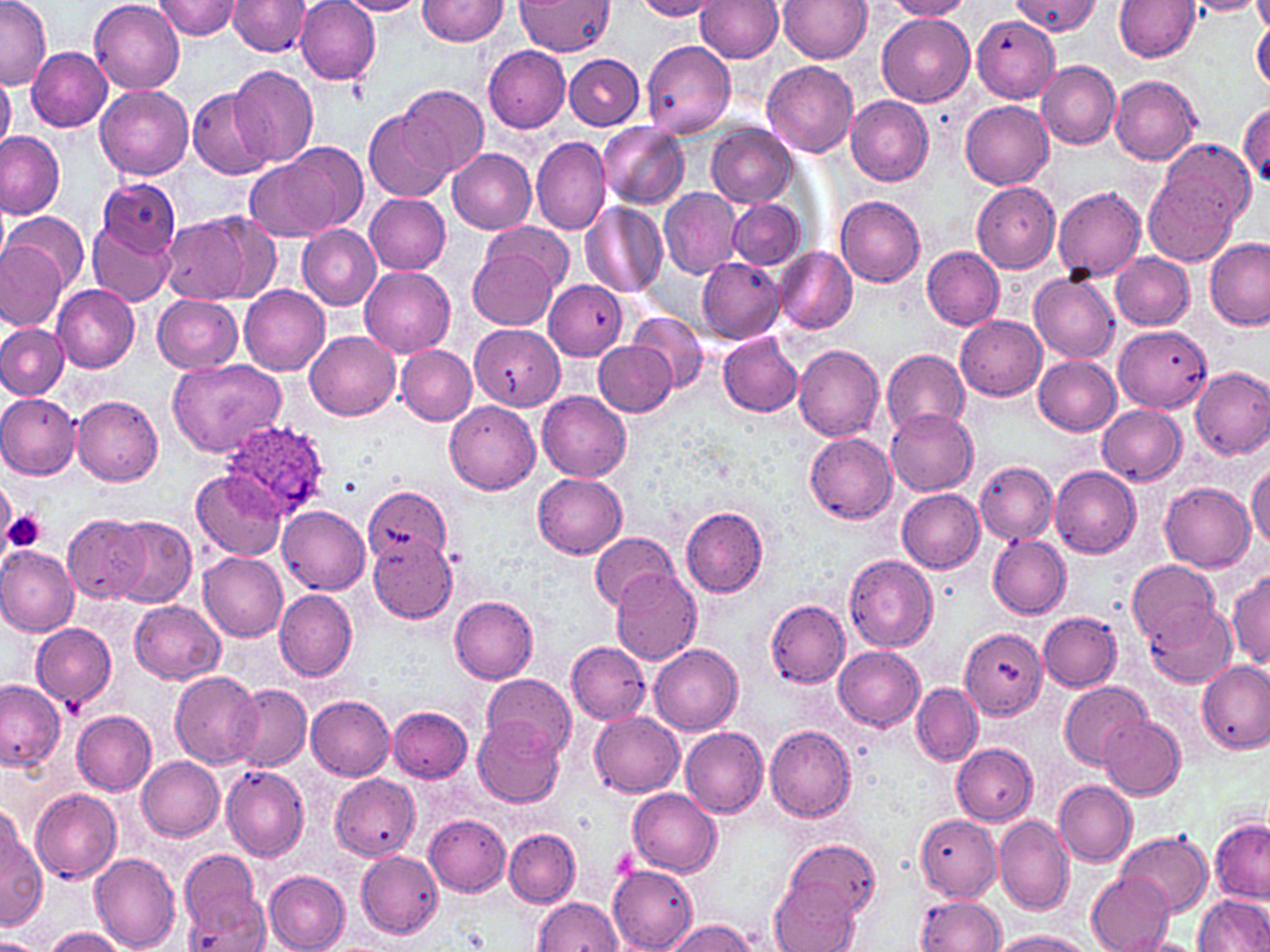
Summary:
  - Coordinate format: approximate bounding boxes as (x1,y1)-(x2,y2) corner pairs in pixels
  - Platelet locations: (0,480)-(15,544), (4,509)-(47,552), (609,845)-(638,883)
  - Plasmodium ovale-infected red blood cell locations: (221,418)-(332,520)
  - Uninfected red blood cell locations: (0,0)-(50,88), (90,0)-(184,93), (157,0)-(239,40), (296,0)-(380,84), (419,0)-(509,46), (517,0)-(614,56), (635,0)-(724,21), (778,0)-(873,63), (883,0)-(977,20), (1014,0)-(1100,35), (1114,0)-(1200,62), (1187,0)-(1267,17), (1253,0)-(1270,34), (229,1)-(310,57), (338,1)-(424,17), (697,1)-(784,62), (877,11)-(975,106), (972,15)-(1059,102), (1251,19)-(1270,90), (641,40)-(737,138), (26,46)-(114,131), (484,46)-(570,132), (565,53)-(643,129), (762,60)-(858,158), (1035,60)-(1120,149), (228,66)-(318,167), (0,73)-(16,148), (1110,74)-(1202,166), (97,84)-(194,180), (396,84)-(487,178), (189,89)-(275,178), (846,95)-(934,185), (961,101)-(1054,190), (1237,101)-(1269,181), (365,110)-(455,201), (596,121)-(689,208), (707,124)-(796,207), (0,132)-(65,218), (530,136)-(611,236), (280,142)-(367,232), (448,148)-(536,234), (245,155)-(346,243), (1145,157)-(1249,267), (98,178)-(180,257), (971,183)-(1061,274), (659,186)-(742,279), (1053,187)-(1147,281), (365,192)-(451,274), (835,195)-(926,288), (728,198)-(804,269), (580,202)-(668,296), (6,213)-(88,291), (161,213)-(254,301), (484,220)-(572,293), (89,221)-(175,307), (297,223)-(381,310), (1204,237)-(1269,329), (0,241)-(67,330), (471,244)-(560,330), (921,245)-(1004,330), (773,246)-(857,335), (1111,253)-(1195,330), (698,257)-(785,345), (359,266)-(455,357), (1030,272)-(1120,363), (544,279)-(625,360), (53,284)-(140,372), (240,285)-(330,375), (153,294)-(243,374), (627,311)-(709,394), (956,315)-(1047,400), (0,323)-(69,400), (470,325)-(568,412), (1114,325)-(1212,412), (306,331)-(399,420), (718,333)-(803,416), (594,340)-(675,416), (794,344)-(884,441), (397,346)-(476,425), (881,348)-(971,437), (1034,356)-(1121,436), (170,358)-(285,456), (1190,365)-(1270,460), (537,390)-(632,482), (0,393)-(81,480), (72,393)-(164,486), (445,402)-(540,495), (1097,405)-(1186,485), (887,406)-(978,495), (804,431)-(898,523), (975,461)-(1056,544), (1247,462)-(1270,550), (1049,466)-(1140,557), (192,469)-(286,561), (533,474)-(627,558), (1160,483)-(1255,571), (337,485)-(456,573), (897,489)-(985,573), (682,505)-(770,597), (279,506)-(370,592), (63,513)-(151,604), (108,516)-(196,608), (590,532)-(677,609), (987,534)-(1071,617), (367,535)-(457,622), (0,546)-(79,637), (199,552)-(288,641), (844,555)-(938,652), (1128,560)-(1220,644), (610,565)-(701,666), (1227,570)-(1270,670), (275,589)-(357,680), (449,596)-(538,683), (131,600)-(226,684), (765,600)-(849,687), (1143,603)-(1235,686), (1040,612)-(1121,691), (31,624)-(116,707), (959,629)-(1047,719), (566,641)-(650,724), (648,643)-(743,734), (834,646)-(925,731), (1197,659)-(1269,756), (171,671)-(262,768), (484,674)-(577,756), (0,680)-(66,771), (1060,682)-(1152,769), (913,683)-(983,765), (231,686)-(311,770), (307,696)-(396,780), (389,706)-(472,782), (73,710)-(157,795), (590,712)-(684,797), (1097,713)-(1184,799), (473,717)-(563,806), (765,724)-(856,823), (681,726)-(769,816), (951,743)-(1038,825), (137,756)-(224,841), (222,766)-(308,862), (330,773)-(421,861), (1053,781)-(1136,867), (627,787)-(721,876), (30,788)-(122,884), (423,811)-(511,896), (915,814)-(1002,900), (996,814)-(1073,917), (0,816)-(45,931), (1210,818)-(1268,902), (504,828)-(581,907), (1116,831)-(1212,919), (784,837)-(882,920), (89,850)-(180,951), (358,850)-(443,938), (179,851)-(266,949), (608,866)-(697,951), (264,870)-(350,952), (1088,872)-(1174,952), (771,878)-(862,951), (914,895)-(1006,950), (1195,895)-(1270,950), (533,898)-(624,952), (664,919)-(757,952), (40,928)-(130,952), (991,931)-(1094,952), (1122,937)-(1201,952), (0,938)-(44,952)
  - Slide-level diagnosis: Plasmodium ovale
  - Preparation: thin blood film
  - Modality: optical microscopy
  - Magnification: 1000x
  - Stain: May-Grünwald-Giemsa
  - Field of view: single
  - Image size: 1270×952 pixels